Assess this cell for malaria.
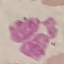

It is uninfected.

{
  "image_type": "automatically extracted cell patch, resized to 64 × 64 pixels",
  "preparation": "thin blood film",
  "capture": "smartphone through the microscope eyepiece",
  "stain": "Giemsa"
}